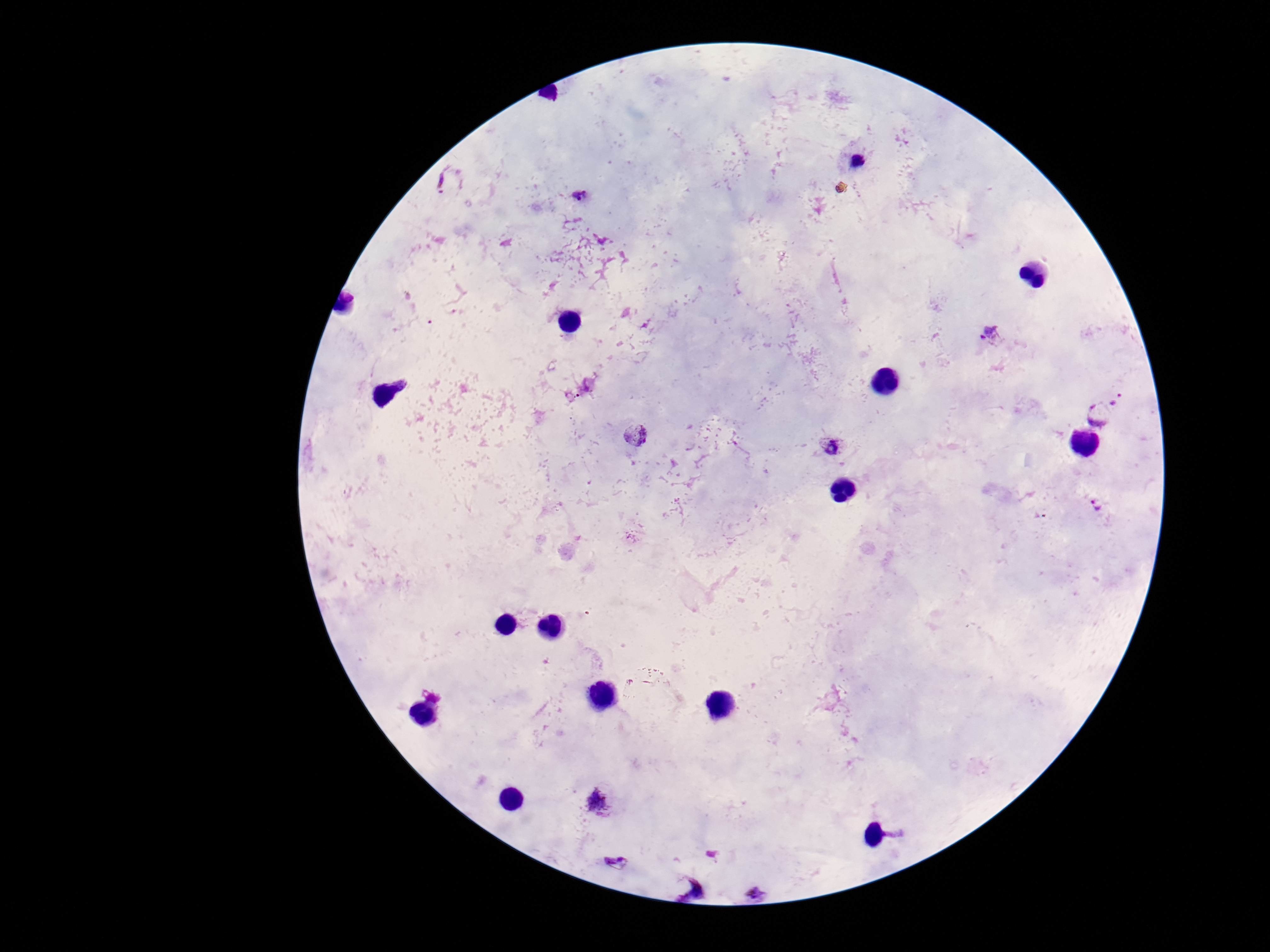
{
  "patient_malaria_status": "positive",
  "field_of_view": "one from this slide",
  "stain": "Giemsa",
  "image_size": "1270×952 pixels",
  "plasmodium_parasite_locations": "approximate centers as [x, y] in pixels: [857, 164], [450, 180], [578, 195], [992, 335], [1118, 399], [1097, 415], [636, 436], [830, 447], [1099, 505], [597, 802], [619, 862], [689, 888], [755, 894]",
  "magnification": "100x",
  "preparation": "thick blood smear",
  "capture": "smartphone camera through the microscope eyepiece"
}